Assess this cell for malaria.
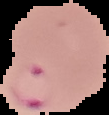

Parasitized.

Image is 109×115 pixels. From a thin blood smear. Segmented cell region on a black background.